Name the parasite shown.
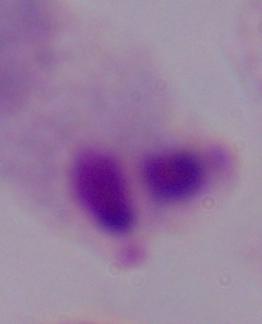

This is a trichomonad.

Photomicrograph. Captured at 1000x magnification.